Report the malaria status of this cell.
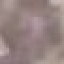

Uninfected.

{
  "image_type": "cell patch, automatically extracted from a larger field of view and resized to 64 × 64 pixels",
  "preparation": "thin blood smear",
  "capture": "smartphone through the microscope eyepiece",
  "stain": "Giemsa"
}